Report the malaria status of this cell.
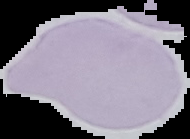

Uninfected.

From a thin blood smear. Image is 190×139 pixels. Cell region segmented out of the field of view; the surrounding area is masked to black.